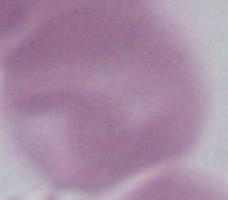

Photomicrograph. 1000x magnification. A red blood cell is shown.